Comment on the background quality.
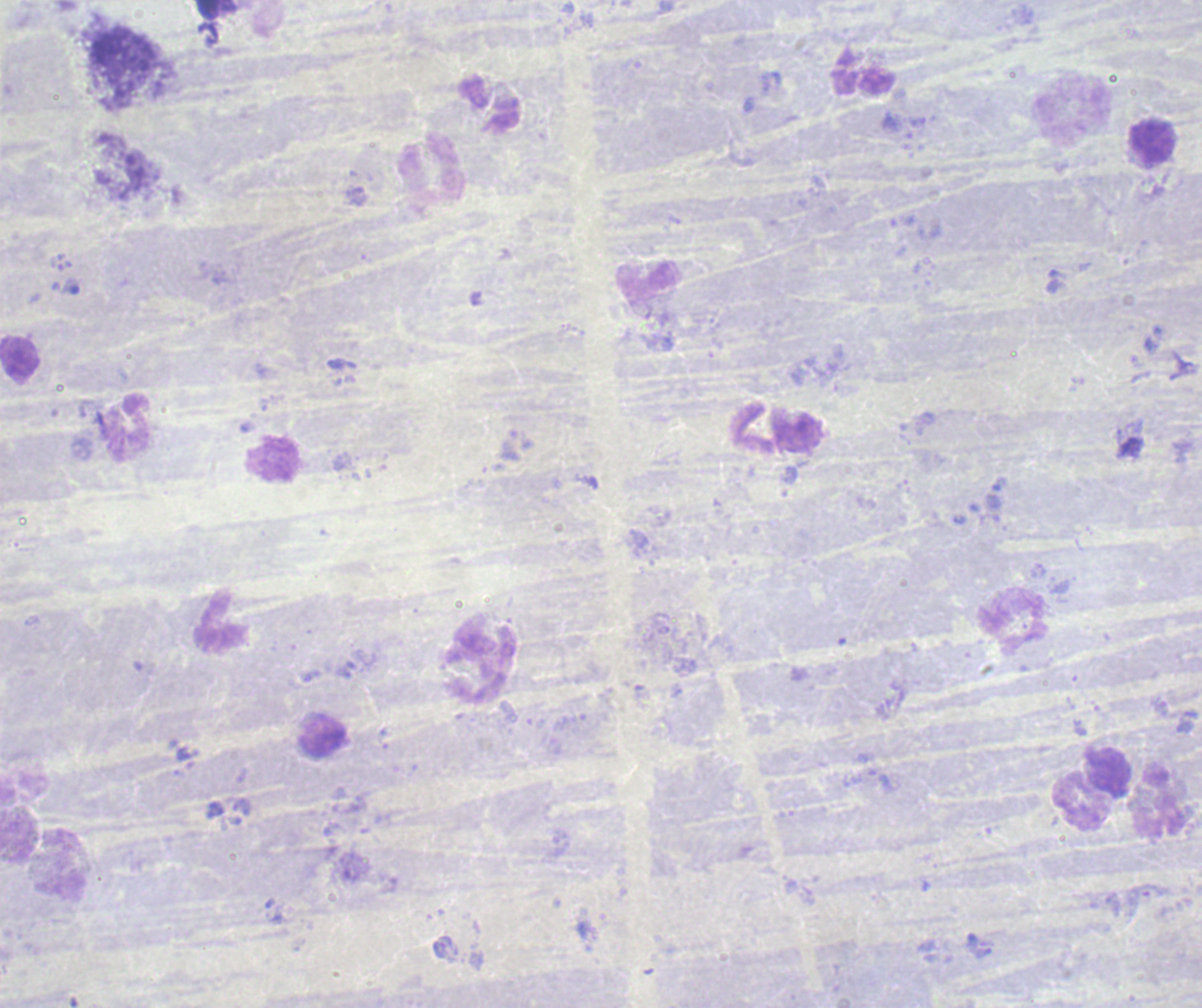

Poor.

Approximate centers as {x, y} in pixels.
Summary:
  - Leukocyte locations: {1072, 111}, {1154, 145}, {432, 172}, {126, 428}, {1012, 621}, {222, 623}, {478, 672}, {323, 735}, {1107, 769}, {1080, 800}, {1161, 802}
  - Context: previously used in an actual diagnosis
  - Result: no malaria parasites seen
  - Field of view: single
  - Magnification: 100x
  - Image size: 1202×1008 pixels
  - Stain: Romanowsky
  - Preparation: thick smear of blood